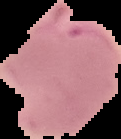

image type = cell region segmented out of the field of view; surrounding area masked to black
image size = 121×139 pixels
preparation = thin blood film
result = Plasmodium parasites detected